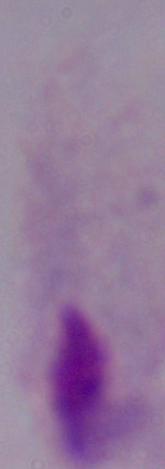
{
  "modality": "micrograph",
  "magnification": "1000x",
  "identification": "trichomonad"
}